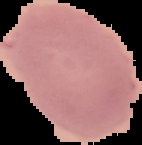 The area outside the segmented cell region is set to black. Result: no malaria parasites detected. Image is 142×145 pixels. From a thin blood smear.